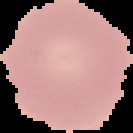

Image is 133×133 pixels. From a thin blood film. Cell region segmented out of the field of view; the surrounding area is masked to black. Malaria status: uninfected.